Assess the morphology of the red blood cells.
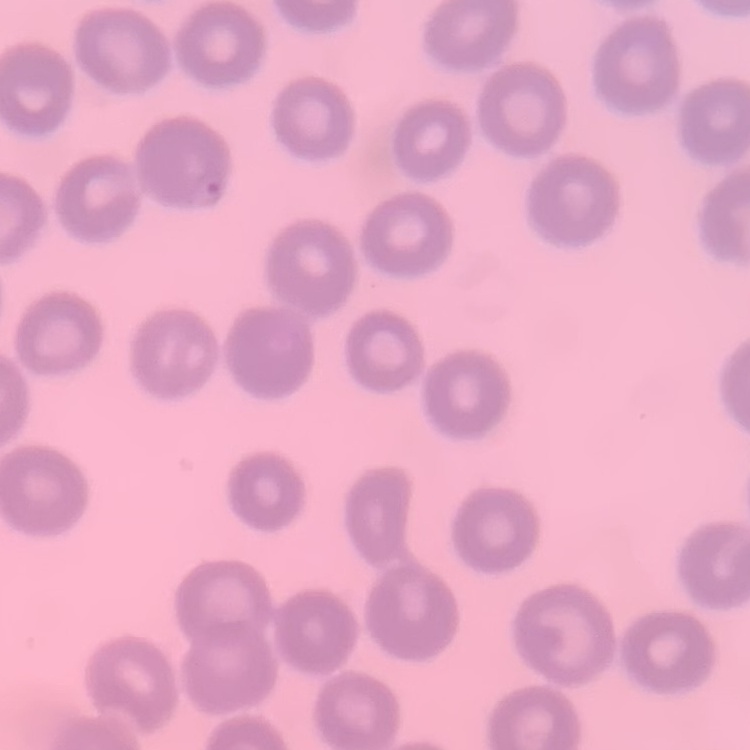
They show no rouleaux formation.

Field's or Giemsa stain. Thin blood film. One tile cut from a larger photomicrograph.